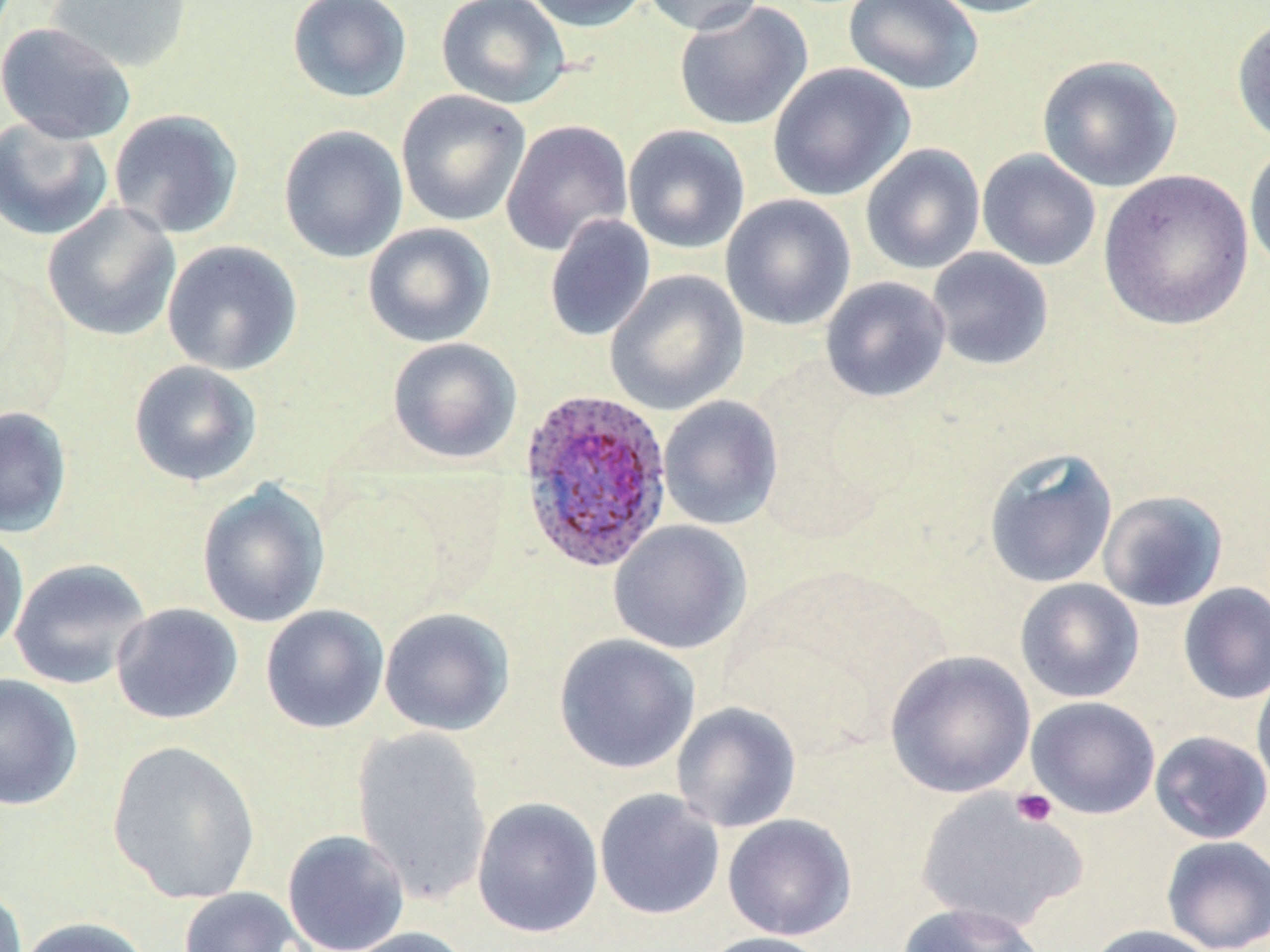
Approximate bounding boxes as named x1/y1/x2/y2 corners in pixels. Uninfected red blood cell locations: (x1=46, y1=0, x2=194, y2=74), (x1=287, y1=0, x2=413, y2=104), (x1=436, y1=0, x2=571, y2=109), (x1=519, y1=0, x2=652, y2=33), (x1=640, y1=0, x2=768, y2=35), (x1=843, y1=0, x2=984, y2=95), (x1=924, y1=0, x2=1063, y2=18), (x1=673, y1=1, x2=813, y2=131), (x1=1231, y1=14, x2=1270, y2=147), (x1=0, y1=21, x2=136, y2=145), (x1=1036, y1=54, x2=1182, y2=192), (x1=767, y1=63, x2=915, y2=202), (x1=396, y1=89, x2=531, y2=227), (x1=108, y1=109, x2=244, y2=239), (x1=0, y1=115, x2=114, y2=241), (x1=501, y1=119, x2=634, y2=256), (x1=278, y1=124, x2=408, y2=263), (x1=622, y1=124, x2=751, y2=254), (x1=1244, y1=139, x2=1270, y2=276), (x1=860, y1=143, x2=986, y2=275), (x1=976, y1=149, x2=1101, y2=272), (x1=1098, y1=169, x2=1255, y2=331), (x1=720, y1=194, x2=856, y2=331), (x1=41, y1=202, x2=182, y2=342), (x1=544, y1=214, x2=656, y2=342), (x1=362, y1=223, x2=496, y2=347), (x1=162, y1=240, x2=303, y2=376), (x1=926, y1=247, x2=1053, y2=371), (x1=604, y1=269, x2=749, y2=415), (x1=820, y1=276, x2=951, y2=402), (x1=386, y1=337, x2=522, y2=465), (x1=128, y1=360, x2=263, y2=487), (x1=658, y1=395, x2=783, y2=531), (x1=0, y1=405, x2=72, y2=537), (x1=982, y1=447, x2=1118, y2=589), (x1=196, y1=481, x2=331, y2=629), (x1=1097, y1=489, x2=1228, y2=612), (x1=608, y1=520, x2=752, y2=655), (x1=0, y1=526, x2=29, y2=658), (x1=9, y1=557, x2=151, y2=690), (x1=1015, y1=578, x2=1144, y2=703), (x1=1178, y1=582, x2=1270, y2=704), (x1=110, y1=603, x2=243, y2=725), (x1=260, y1=604, x2=390, y2=734), (x1=379, y1=607, x2=515, y2=736), (x1=553, y1=633, x2=700, y2=774), (x1=884, y1=650, x2=1036, y2=798), (x1=1252, y1=665, x2=1270, y2=799), (x1=0, y1=673, x2=83, y2=811), (x1=1026, y1=696, x2=1160, y2=819), (x1=671, y1=701, x2=802, y2=833), (x1=351, y1=727, x2=493, y2=904), (x1=1150, y1=730, x2=1270, y2=844), (x1=106, y1=739, x2=262, y2=905), (x1=594, y1=788, x2=725, y2=920), (x1=916, y1=789, x2=1087, y2=934), (x1=471, y1=797, x2=604, y2=938), (x1=722, y1=813, x2=857, y2=940), (x1=281, y1=829, x2=411, y2=952), (x1=1161, y1=835, x2=1270, y2=952), (x1=0, y1=881, x2=27, y2=952), (x1=178, y1=886, x2=312, y2=952), (x1=895, y1=902, x2=1048, y2=952), (x1=16, y1=916, x2=152, y2=952), (x1=1086, y1=924, x2=1219, y2=952), (x1=338, y1=926, x2=476, y2=952), (x1=697, y1=931, x2=838, y2=952). Platelet locations: (x1=1011, y1=788, x2=1057, y2=828). Plasmodium ovale-infected red blood cell locations: (x1=517, y1=387, x2=674, y2=576). Slide-level diagnosis: Plasmodium ovale. Thin blood smear. Optical microscopy. Image is 1270×952 pixels. May-Grünwald-Giemsa stain. One field of a larger specimen. 1000x magnification.